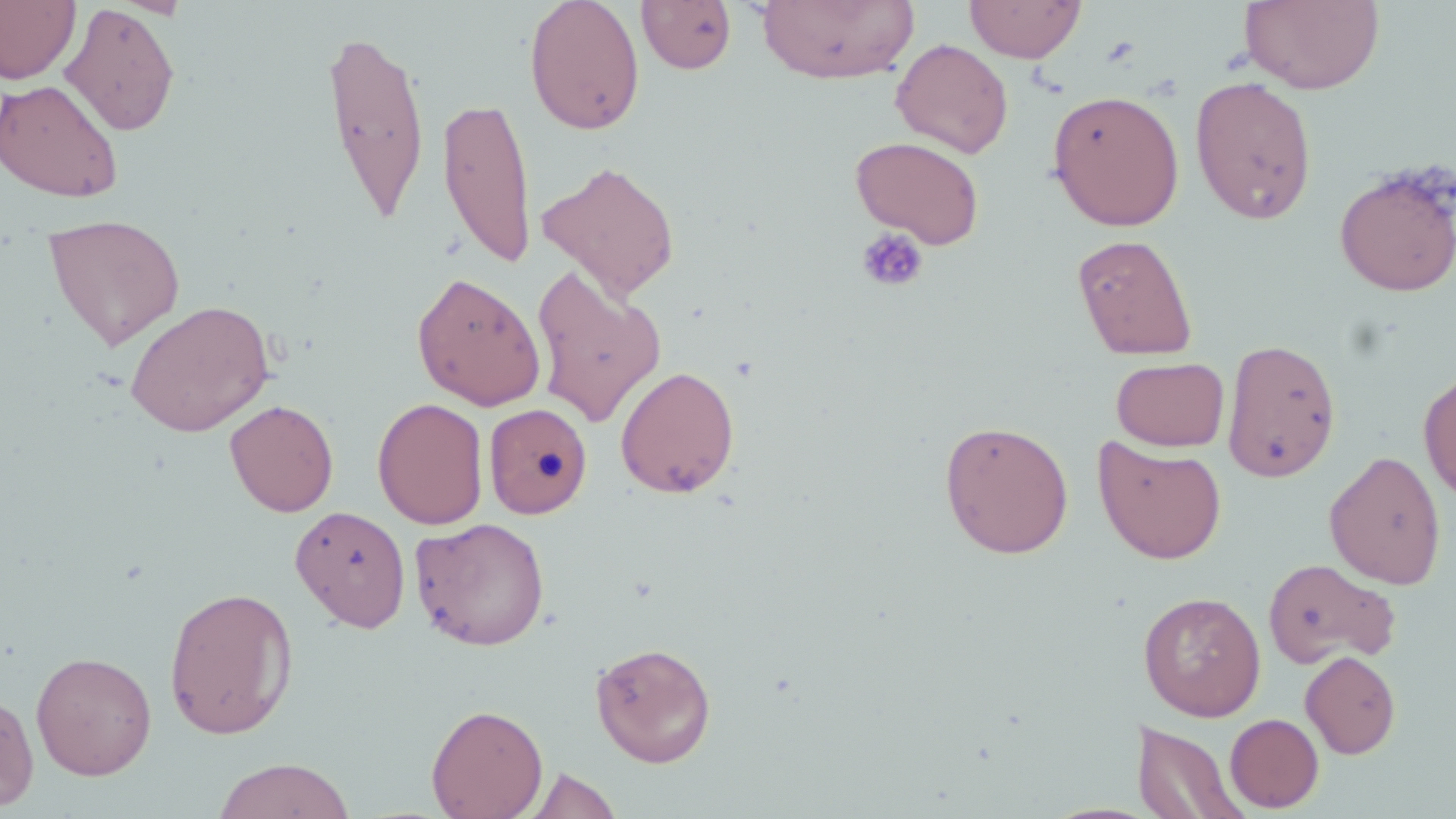

Summary:
  - Coordinate format: approximate bounding boxes as (x1,y1)-(x2,y2) corner pairs in pixels
  - Platelet locations: (855,226)-(929,293)
  - Uninfected red blood cell locations: (0,0)-(80,85), (523,0)-(646,136), (964,0)-(1086,63), (636,1)-(737,74), (755,1)-(918,84), (1240,1)-(1385,95), (60,3)-(181,136), (319,25)-(432,227), (891,38)-(1013,158), (1189,76)-(1318,225), (0,79)-(124,202), (1047,89)-(1185,230), (435,96)-(537,270), (850,135)-(985,249), (537,160)-(681,301), (1333,162)-(1456,297), (42,213)-(185,350), (1072,233)-(1198,361), (531,266)-(667,428), (410,271)-(546,411), (125,299)-(275,437), (1221,337)-(1342,483), (1111,357)-(1229,451), (615,365)-(740,498), (1419,371)-(1456,503), (372,397)-(489,529), (225,399)-(339,517), (484,403)-(592,519), (938,419)-(1074,558), (1093,437)-(1228,565), (1324,450)-(1447,590), (290,505)-(411,632), (409,516)-(551,651), (1262,558)-(1399,668), (163,585)-(299,740), (1138,590)-(1266,721), (590,640)-(717,767), (30,651)-(157,780), (1300,651)-(1401,759), (0,689)-(39,813), (426,702)-(548,818), (1225,713)-(1323,812), (1133,718)-(1248,819), (213,757)-(355,819), (523,767)-(622,819)
  - Slide-level diagnosis: no evidence of blood parasites
  - Field of view: single
  - Preparation: thin blood film
  - Image size: 1456×819 pixels
  - Modality: optical microscopy
  - Stain: May-Grünwald-Giemsa
  - Magnification: 1000x